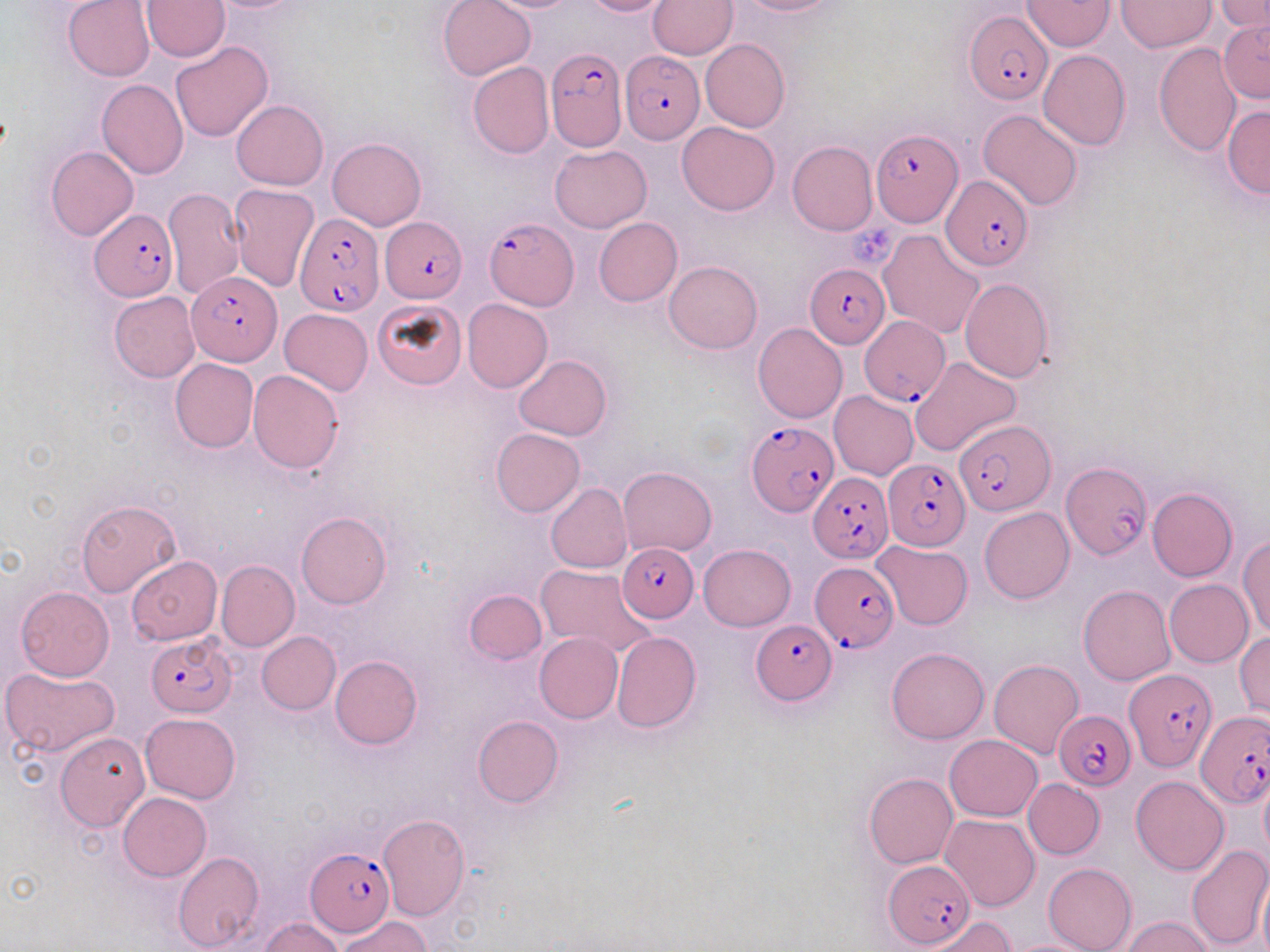
slide-level diagnosis = Plasmodium falciparum
image size = 1270×952 pixels
magnification = 1000x
Plasmodium falciparum-infected red blood cell locations = approximate bounding boxes as named x1/y1/x2/y2 corners in pixels: (x1=965, y1=10, x2=1051, y2=103), (x1=544, y1=46, x2=628, y2=150), (x1=620, y1=51, x2=705, y2=146), (x1=871, y1=130, x2=962, y2=228), (x1=940, y1=176, x2=1032, y2=272), (x1=89, y1=210, x2=178, y2=301), (x1=295, y1=213, x2=382, y2=317), (x1=486, y1=217, x2=578, y2=311), (x1=380, y1=218, x2=467, y2=303), (x1=806, y1=264, x2=891, y2=349), (x1=186, y1=271, x2=283, y2=365), (x1=860, y1=318, x2=948, y2=404), (x1=745, y1=419, x2=838, y2=516), (x1=956, y1=419, x2=1053, y2=514), (x1=886, y1=459, x2=970, y2=548), (x1=1061, y1=463, x2=1150, y2=560), (x1=808, y1=473, x2=892, y2=565), (x1=617, y1=543, x2=698, y2=620), (x1=812, y1=560, x2=899, y2=652), (x1=751, y1=617, x2=839, y2=706), (x1=147, y1=633, x2=238, y2=717), (x1=1122, y1=665, x2=1214, y2=772), (x1=1053, y1=710, x2=1135, y2=790), (x1=1197, y1=711, x2=1269, y2=808), (x1=306, y1=849, x2=394, y2=935), (x1=883, y1=861, x2=977, y2=949)
stain = May-Grünwald-Giemsa
modality = optical microscopy
platelet locations = approximate bounding boxes as named x1/y1/x2/y2 corners in pixels: (x1=844, y1=217, x2=904, y2=263)
field of view = one of a larger specimen
preparation = thin blood smear
uninfected red blood cell locations = approximate bounding boxes as named x1/y1/x2/y2 corners in pixels: (x1=437, y1=0, x2=536, y2=81), (x1=477, y1=0, x2=586, y2=13), (x1=581, y1=0, x2=672, y2=17), (x1=731, y1=0, x2=841, y2=16), (x1=1116, y1=0, x2=1214, y2=53), (x1=1215, y1=0, x2=1270, y2=33), (x1=63, y1=1, x2=155, y2=82), (x1=141, y1=1, x2=229, y2=61), (x1=647, y1=1, x2=737, y2=59), (x1=1021, y1=1, x2=1114, y2=50), (x1=1217, y1=20, x2=1270, y2=104), (x1=700, y1=38, x2=790, y2=132), (x1=170, y1=41, x2=274, y2=142), (x1=1154, y1=43, x2=1242, y2=157), (x1=1039, y1=50, x2=1130, y2=150), (x1=466, y1=61, x2=555, y2=158), (x1=97, y1=79, x2=188, y2=178), (x1=232, y1=100, x2=328, y2=189), (x1=1223, y1=106, x2=1270, y2=198), (x1=979, y1=109, x2=1083, y2=210), (x1=676, y1=122, x2=780, y2=215), (x1=328, y1=137, x2=426, y2=231), (x1=787, y1=140, x2=877, y2=235), (x1=549, y1=145, x2=652, y2=232), (x1=47, y1=146, x2=139, y2=242), (x1=229, y1=184, x2=320, y2=293), (x1=162, y1=185, x2=245, y2=299), (x1=593, y1=217, x2=682, y2=307), (x1=878, y1=228, x2=985, y2=338), (x1=664, y1=259, x2=763, y2=353), (x1=959, y1=277, x2=1054, y2=381), (x1=110, y1=292, x2=200, y2=382), (x1=462, y1=299, x2=553, y2=392), (x1=373, y1=300, x2=466, y2=390), (x1=279, y1=308, x2=373, y2=395), (x1=753, y1=323, x2=846, y2=422), (x1=513, y1=355, x2=611, y2=441), (x1=170, y1=357, x2=259, y2=452), (x1=910, y1=357, x2=1020, y2=457), (x1=248, y1=370, x2=344, y2=473), (x1=829, y1=391, x2=920, y2=479), (x1=491, y1=428, x2=585, y2=516), (x1=618, y1=465, x2=717, y2=556), (x1=546, y1=483, x2=633, y2=573), (x1=1146, y1=488, x2=1238, y2=581), (x1=75, y1=498, x2=182, y2=598), (x1=979, y1=507, x2=1073, y2=603), (x1=296, y1=512, x2=391, y2=608), (x1=1237, y1=536, x2=1269, y2=639), (x1=872, y1=541, x2=973, y2=630), (x1=699, y1=544, x2=795, y2=631), (x1=127, y1=557, x2=222, y2=645), (x1=215, y1=560, x2=299, y2=652), (x1=535, y1=564, x2=656, y2=658), (x1=1165, y1=579, x2=1253, y2=667), (x1=1078, y1=585, x2=1175, y2=684), (x1=15, y1=586, x2=115, y2=681), (x1=463, y1=589, x2=547, y2=666), (x1=256, y1=631, x2=340, y2=714), (x1=610, y1=631, x2=701, y2=734), (x1=1235, y1=631, x2=1269, y2=720), (x1=534, y1=633, x2=623, y2=723), (x1=885, y1=647, x2=991, y2=743), (x1=331, y1=655, x2=422, y2=749), (x1=989, y1=660, x2=1084, y2=760), (x1=1, y1=666, x2=120, y2=757), (x1=139, y1=713, x2=241, y2=802), (x1=473, y1=715, x2=563, y2=808), (x1=54, y1=732, x2=149, y2=831), (x1=944, y1=734, x2=1043, y2=821), (x1=863, y1=773, x2=958, y2=869), (x1=1131, y1=775, x2=1229, y2=875), (x1=1259, y1=776, x2=1270, y2=856), (x1=1023, y1=779, x2=1105, y2=860), (x1=117, y1=793, x2=211, y2=881), (x1=941, y1=813, x2=1040, y2=911), (x1=377, y1=814, x2=470, y2=920), (x1=1185, y1=844, x2=1270, y2=950), (x1=173, y1=851, x2=264, y2=952), (x1=1043, y1=863, x2=1136, y2=952), (x1=1256, y1=873, x2=1270, y2=952), (x1=924, y1=916, x2=1018, y2=952), (x1=1123, y1=916, x2=1216, y2=952), (x1=259, y1=917, x2=345, y2=951), (x1=337, y1=917, x2=431, y2=951), (x1=1001, y1=938, x2=1104, y2=952)